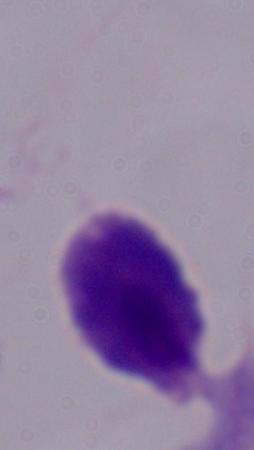
Micrograph. A trichomonad is seen. 1000x magnification.